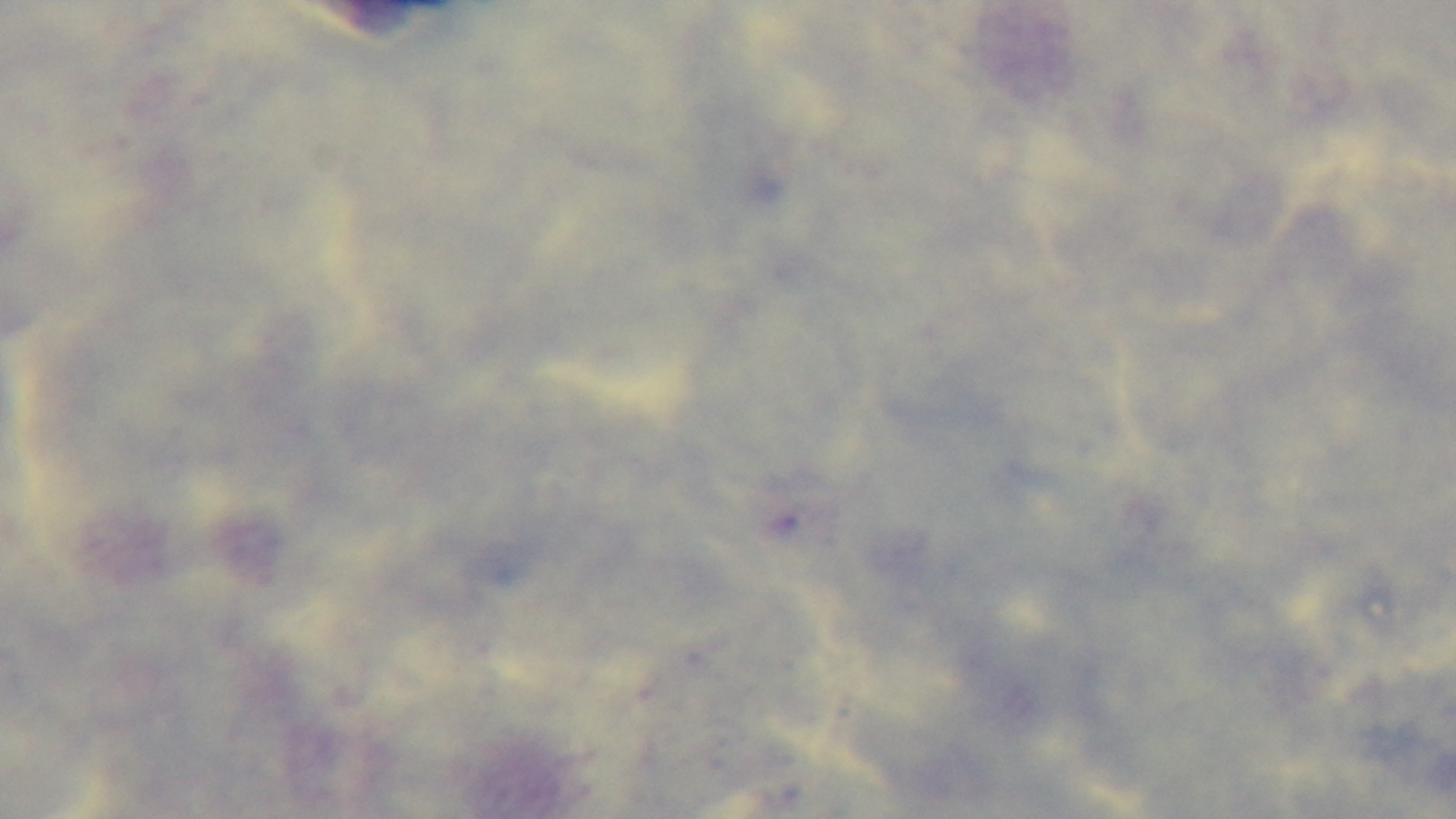

objective: 100x oil immersion
malaria_status: negative
preparation: thick smear
field_of_view: single
stain: Giemsa
capture: mounted 4K digital camera
modality: light microscopy